Report the malaria status of this cell.
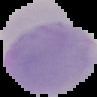

It is uninfected.

Summary:
  - Image type: segmented cell region on a black background
  - Preparation: thin blood film
  - Image size: 97×97 pixels